Locate every blood parasite and identify its species.
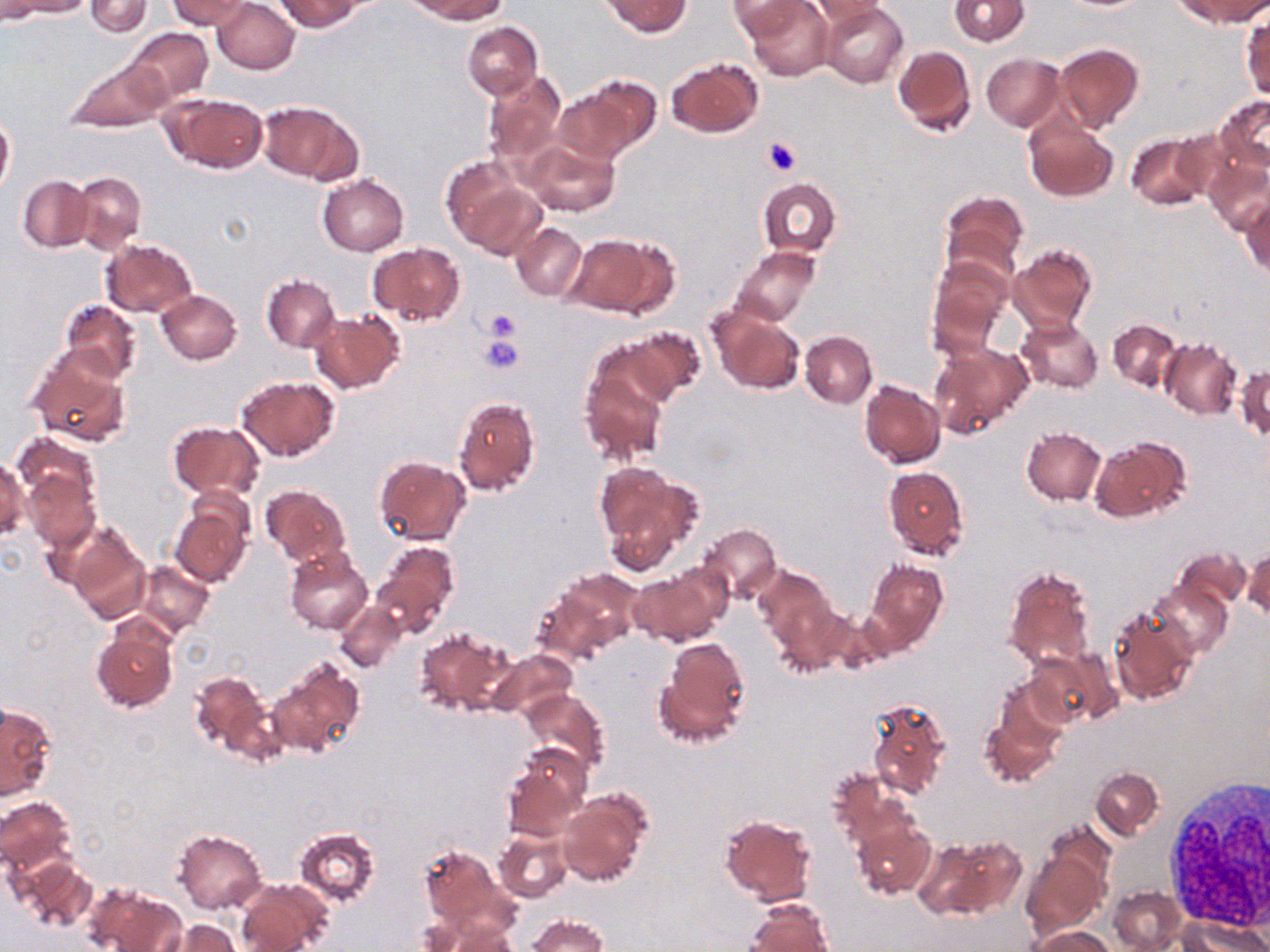
No blood parasites seen.

slide-level diagnosis = negative for blood parasites
preparation = thin blood smear
uninfected red blood cell locations = approximate bounding boxes as (x1,y1)-(x2,y2) corner pairs in pixels: (1,0)-(55,25), (8,0)-(92,18), (84,0)-(152,37), (167,0)-(254,31), (213,0)-(299,74), (276,0)-(362,32), (406,0)-(507,23), (603,0)-(690,37), (745,0)-(835,81), (948,0)-(1029,45), (808,1)-(885,35), (1180,1)-(1268,28), (727,2)-(809,37), (820,2)-(909,88), (1242,15)-(1269,100), (463,22)-(542,99), (124,27)-(214,105), (1055,43)-(1143,134), (892,45)-(977,136), (981,54)-(1063,130), (666,57)-(763,137), (62,58)-(171,131), (483,71)-(566,165), (568,75)-(660,163), (164,93)-(269,173), (1214,95)-(1270,173), (256,101)-(360,184), (0,112)-(15,196), (1024,117)-(1119,202), (1125,132)-(1214,211), (526,140)-(618,216), (438,154)-(528,246), (1203,156)-(1270,235), (71,171)-(146,253), (317,174)-(410,256), (17,175)-(93,251), (757,178)-(841,257), (455,179)-(550,263), (939,190)-(1027,282), (1239,197)-(1269,280), (511,221)-(587,300), (566,231)-(672,317), (100,239)-(197,318), (368,243)-(464,326), (1009,243)-(1097,334), (730,246)-(821,325), (927,259)-(1011,354), (261,274)-(340,352), (156,289)-(242,364), (59,300)-(141,383), (709,308)-(805,395), (310,311)-(404,394), (1015,317)-(1103,394), (1108,319)-(1183,392), (624,326)-(706,405), (800,331)-(877,407), (1160,339)-(1241,419), (930,343)-(1033,436), (29,349)-(132,447), (579,357)-(670,467), (1235,365)-(1269,442), (236,375)-(340,462), (859,380)-(944,468), (453,396)-(540,497), (168,422)-(265,501), (1020,428)-(1106,505), (10,432)-(101,511), (1089,436)-(1190,523), (374,455)-(470,545), (0,456)-(27,542), (597,465)-(699,566), (882,465)-(970,560), (23,470)-(99,552), (260,483)-(350,567), (170,503)-(253,588), (67,523)-(150,623), (699,524)-(782,602), (374,541)-(459,635), (1244,546)-(1270,620), (285,547)-(373,634), (1175,547)-(1252,612), (866,559)-(948,651), (135,561)-(214,638), (1002,564)-(1095,670), (755,565)-(835,647), (540,568)-(641,657), (629,568)-(726,646), (1148,575)-(1232,659), (767,593)-(848,678), (334,600)-(407,673), (1107,609)-(1199,707), (91,621)-(178,713), (414,626)-(514,717), (656,638)-(750,746), (1026,649)-(1117,729), (490,650)-(576,721), (269,659)-(365,759), (189,668)-(275,762), (522,689)-(609,775), (867,697)-(951,798), (1,701)-(56,800), (977,701)-(1062,789), (502,745)-(589,839), (1090,766)-(1163,838), (827,767)-(915,847), (557,792)-(650,886), (0,797)-(76,879), (720,815)-(818,906), (853,819)-(935,898), (1043,820)-(1115,889), (294,826)-(382,908), (172,828)-(266,914), (494,828)-(572,903), (917,833)-(1021,920), (419,843)-(512,939), (1023,849)-(1106,933), (12,855)-(97,933), (237,879)-(332,952), (86,884)-(185,952), (1109,885)-(1186,952), (746,901)-(833,952), (421,912)-(519,952), (528,915)-(607,952), (1181,915)-(1267,952), (160,919)-(239,952), (1031,927)-(1115,952)
image size = 1270×952 pixels
modality = optical microscopy
stain = May-Grünwald-Giemsa
platelet locations = approximate bounding boxes as (x1,y1)-(x2,y2) corner pairs in pixels: (764,136)-(801,175), (483,307)-(523,343), (479,333)-(525,375)
field of view = single
white blood cell locations = approximate bounding boxes as (x1,y1)-(x2,y2) corner pairs in pixels: (1161,779)-(1270,931)
magnification = 1000x